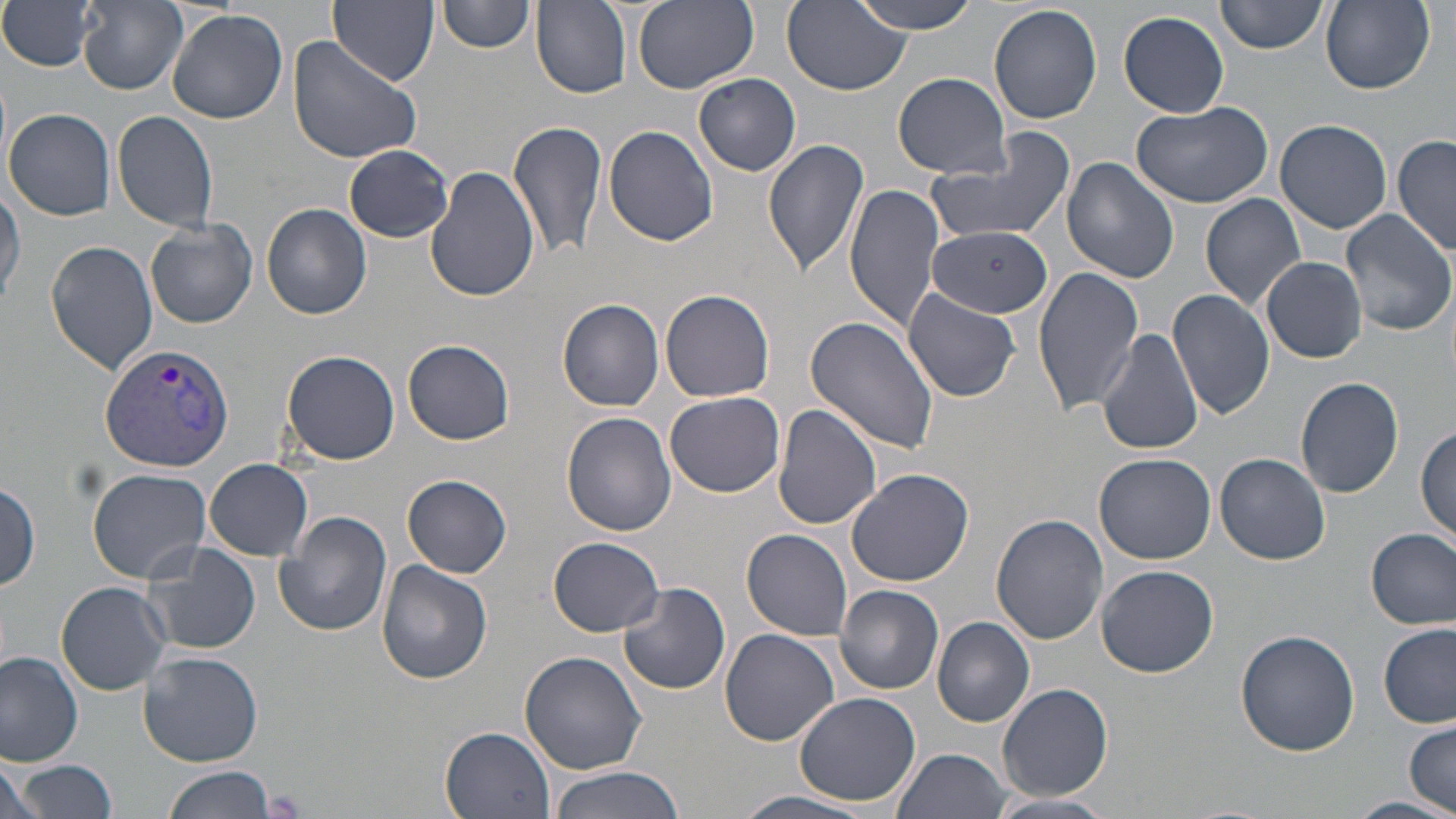

{
  "slide_level_diagnosis": "Plasmodium vivax",
  "field_of_view": "one of a larger specimen",
  "image_size": "1456×819 pixels",
  "magnification": "1000x",
  "plasmodium_vivax_infected_red_blood_cell_locations": "approximate bounding boxes as [x1, y1, x2, y2] in pixels: [100, 343, 236, 471]",
  "preparation": "thin blood smear",
  "uninfected_red_blood_cell_locations": "approximate bounding boxes as [x1, y1, x2, y2] in pixels: [1, 0, 101, 73], [330, 0, 438, 84], [441, 0, 534, 53], [632, 0, 758, 92], [783, 0, 909, 96], [850, 0, 983, 34], [1217, 0, 1329, 55], [1319, 0, 1435, 94], [79, 1, 187, 93], [531, 2, 633, 99], [989, 3, 1103, 125], [167, 9, 290, 125], [1118, 10, 1229, 118], [287, 32, 426, 163], [892, 72, 1013, 179], [695, 73, 801, 176], [1130, 100, 1275, 208], [6, 108, 116, 220], [112, 109, 219, 233], [511, 117, 609, 262], [1275, 118, 1393, 234], [603, 125, 719, 246], [929, 131, 1076, 249], [1393, 135, 1454, 260], [762, 136, 870, 278], [344, 145, 455, 241], [1062, 156, 1180, 285], [427, 168, 539, 304], [0, 183, 24, 309], [844, 183, 945, 332], [1201, 192, 1307, 312], [262, 204, 372, 319], [1339, 208, 1453, 337], [145, 218, 259, 329], [926, 227, 1053, 317], [46, 241, 159, 375], [1260, 257, 1367, 364], [1032, 264, 1145, 415], [901, 287, 1022, 403], [661, 288, 776, 402], [1169, 289, 1275, 420], [558, 298, 664, 412], [806, 316, 940, 453], [1096, 328, 1204, 456], [403, 339, 515, 445], [280, 350, 400, 465], [1296, 376, 1405, 498], [665, 392, 786, 497], [774, 405, 883, 534], [562, 412, 678, 537], [1416, 424, 1455, 546], [1214, 453, 1331, 566], [1095, 454, 1215, 564], [205, 458, 314, 560], [847, 467, 976, 588], [87, 468, 213, 583], [403, 474, 512, 577], [1, 479, 42, 592], [274, 510, 393, 637], [991, 514, 1108, 646], [1368, 527, 1455, 631], [741, 529, 853, 641], [548, 537, 664, 635], [142, 542, 261, 657], [377, 559, 493, 684], [1096, 565, 1218, 676], [56, 582, 171, 694], [618, 583, 731, 694], [834, 584, 943, 695], [932, 616, 1037, 727], [1378, 622, 1454, 729], [719, 628, 840, 748], [1235, 628, 1361, 756], [519, 650, 647, 774], [140, 651, 264, 766], [0, 652, 83, 767], [996, 682, 1114, 801], [795, 692, 922, 805], [1404, 718, 1456, 813], [441, 726, 556, 819], [892, 748, 1012, 819], [0, 759, 46, 819], [20, 759, 116, 817], [163, 764, 278, 819], [547, 767, 686, 819], [729, 791, 882, 819], [982, 792, 1120, 819], [1342, 797, 1456, 819]",
  "stain": "May-Grünwald-Giemsa",
  "modality": "light microscopy"
}